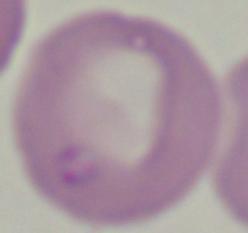

identification = Babesia
magnification = 1000x
modality = photomicrograph